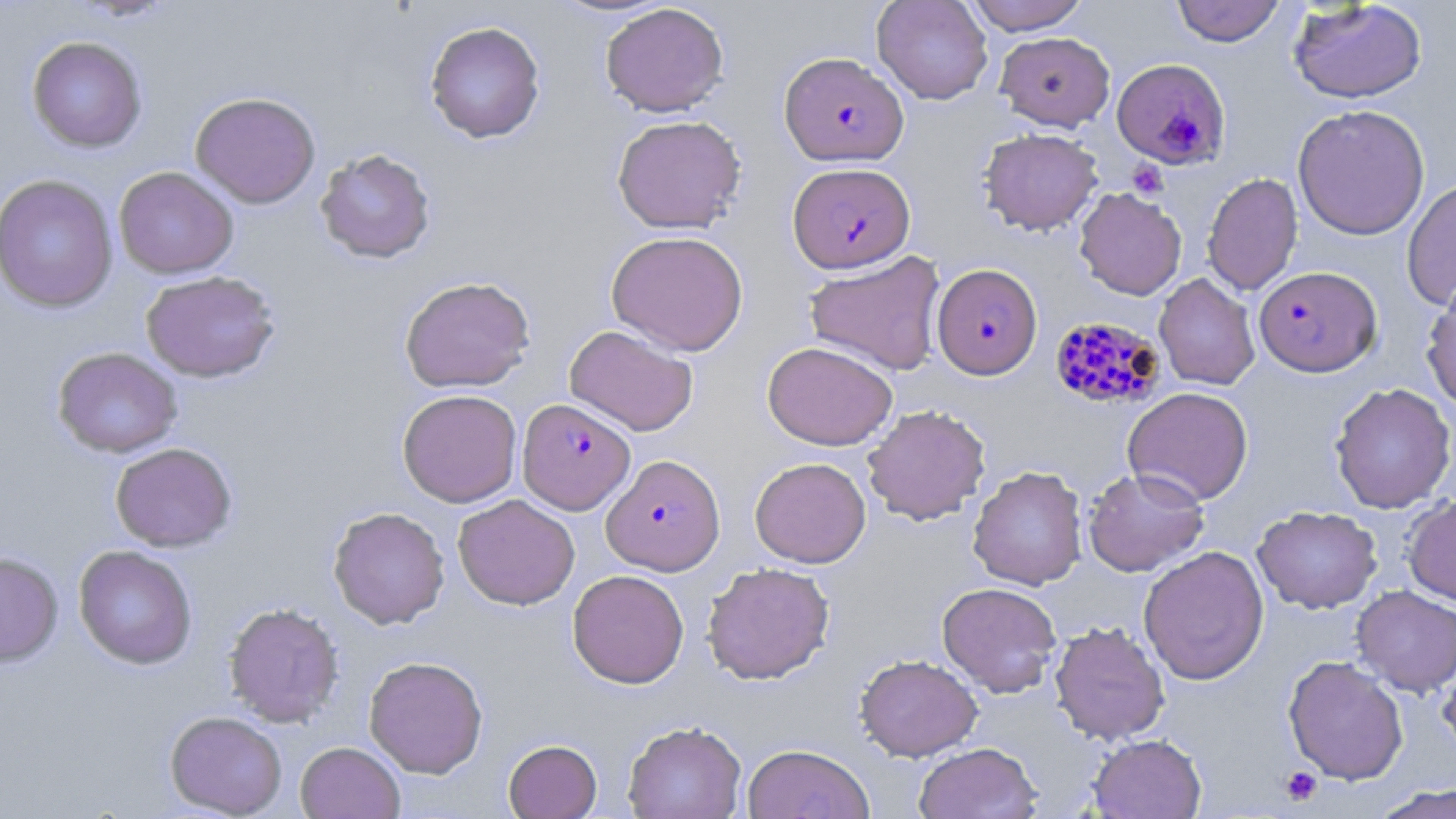
{
  "slide_level_diagnosis": "Plasmodium falciparum",
  "field_of_view": "single",
  "modality": "light microscopy",
  "preparation": "thin blood film",
  "image_size": "1456×819 pixels",
  "uninfected_red_blood_cell_locations": "approximate bounding boxes as (x1, y1, x2, y2) in pixels: (872, 0, 993, 105), (965, 0, 1089, 35), (1171, 0, 1286, 46), (1288, 0, 1428, 104), (600, 3, 729, 117), (424, 20, 546, 143), (994, 31, 1115, 131), (26, 35, 147, 152), (190, 91, 320, 209), (1292, 103, 1430, 240), (611, 115, 747, 234), (978, 127, 1103, 235), (314, 148, 436, 264), (114, 166, 239, 279), (1202, 172, 1303, 296), (0, 173, 119, 313), (1401, 177, 1456, 311), (1074, 187, 1187, 300), (606, 230, 749, 356), (804, 251, 946, 376), (140, 270, 281, 382), (1154, 273, 1261, 390), (399, 276, 536, 393), (1421, 280, 1456, 413), (564, 324, 699, 436), (762, 341, 898, 451), (52, 347, 182, 458), (1329, 382, 1456, 513), (1122, 386, 1254, 506), (397, 389, 522, 507), (862, 404, 991, 525), (110, 442, 237, 552), (749, 457, 871, 568), (968, 466, 1088, 590), (1083, 467, 1210, 576), (452, 493, 580, 610), (1404, 494, 1456, 608), (328, 506, 450, 629), (1252, 506, 1382, 614), (74, 545, 198, 670), (1138, 545, 1270, 685), (0, 552, 63, 667), (701, 561, 836, 685), (567, 569, 689, 688), (937, 581, 1062, 697), (1351, 584, 1456, 697), (223, 602, 344, 727), (1049, 621, 1170, 745), (855, 653, 983, 761), (1437, 654, 1456, 762), (1283, 655, 1409, 785), (363, 656, 488, 778), (165, 710, 287, 818), (622, 720, 747, 819), (1088, 733, 1207, 818), (503, 739, 602, 819), (295, 741, 405, 819), (914, 742, 1041, 819), (742, 743, 874, 819), (1370, 783, 1456, 819)",
  "stain": "May-Grünwald-Giemsa",
  "magnification": "1000x",
  "platelet_locations": "approximate bounding boxes as (x1, y1, x2, y2) in pixels: (1127, 160, 1168, 198), (1280, 766, 1323, 806)",
  "plasmodium_falciparum_infected_red_blood_cell_locations": "approximate bounding boxes as (x1, y1, x2, y2) in pixels: (779, 52, 909, 166), (1111, 57, 1231, 169), (787, 161, 915, 274), (932, 263, 1042, 380), (1253, 265, 1382, 377), (1049, 315, 1166, 411), (517, 398, 635, 514), (601, 454, 725, 575)"
}